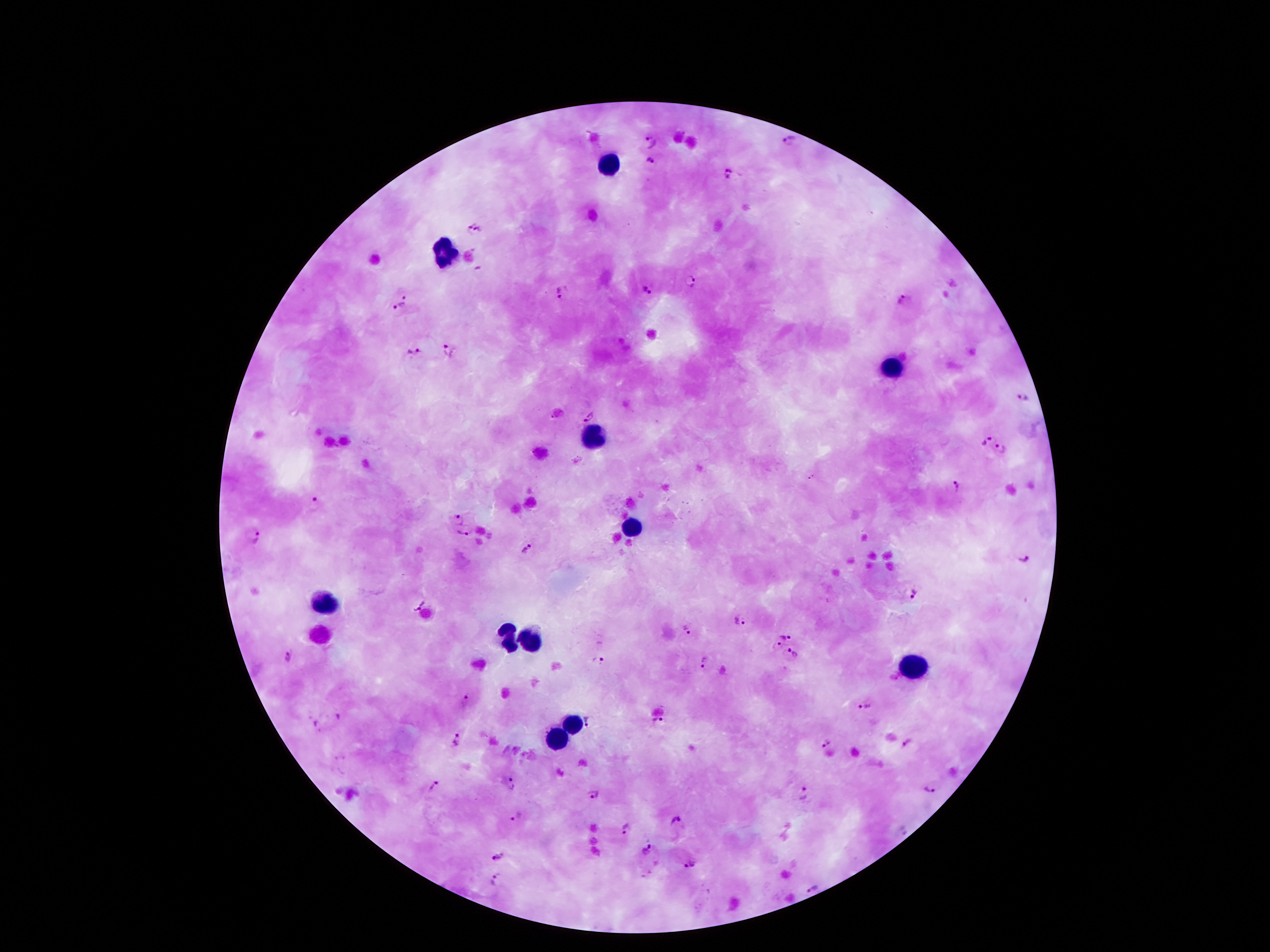

Approximate centers as {x, y} in pixels. Plasmodium parasite locations: {649, 142}, {789, 143}, {650, 163}, {728, 174}, {466, 227}, {481, 229}, {690, 280}, {648, 288}, {563, 293}, {407, 296}, {903, 300}, {399, 306}, {450, 350}, {414, 353}, {1023, 397}, {588, 417}, {985, 440}, {1000, 450}, {956, 486}, {316, 504}, {456, 518}, {466, 532}, {254, 536}, {527, 548}, {1026, 563}, {915, 594}, {415, 602}, {741, 621}, {687, 630}, {786, 633}, {777, 648}, {794, 654}, {288, 658}, {599, 662}, {703, 662}, {464, 702}, {865, 705}, {339, 716}, {657, 720}, {590, 723}, {316, 726}, {456, 742}, {826, 743}, {908, 743}, {512, 784}, {435, 786}, {931, 788}, {803, 794}, {594, 795}, {516, 816}, {676, 821}, {628, 828}, {903, 830}, {648, 848}, {496, 856}, {691, 863}, {497, 879}, {811, 889}. Leukocyte locations: {610, 163}, {444, 251}, {891, 367}, {589, 440}, {631, 528}, {325, 602}, {505, 638}, {532, 640}, {914, 667}, {570, 724}, {555, 739}. Patient malaria status: positive for Plasmodium falciparum. Single field of view. 100x magnification. Smartphone photograph taken through the microscope eyepiece. Image is 1270×952 pixels. Thick blood film. Giemsa-stained preparation.